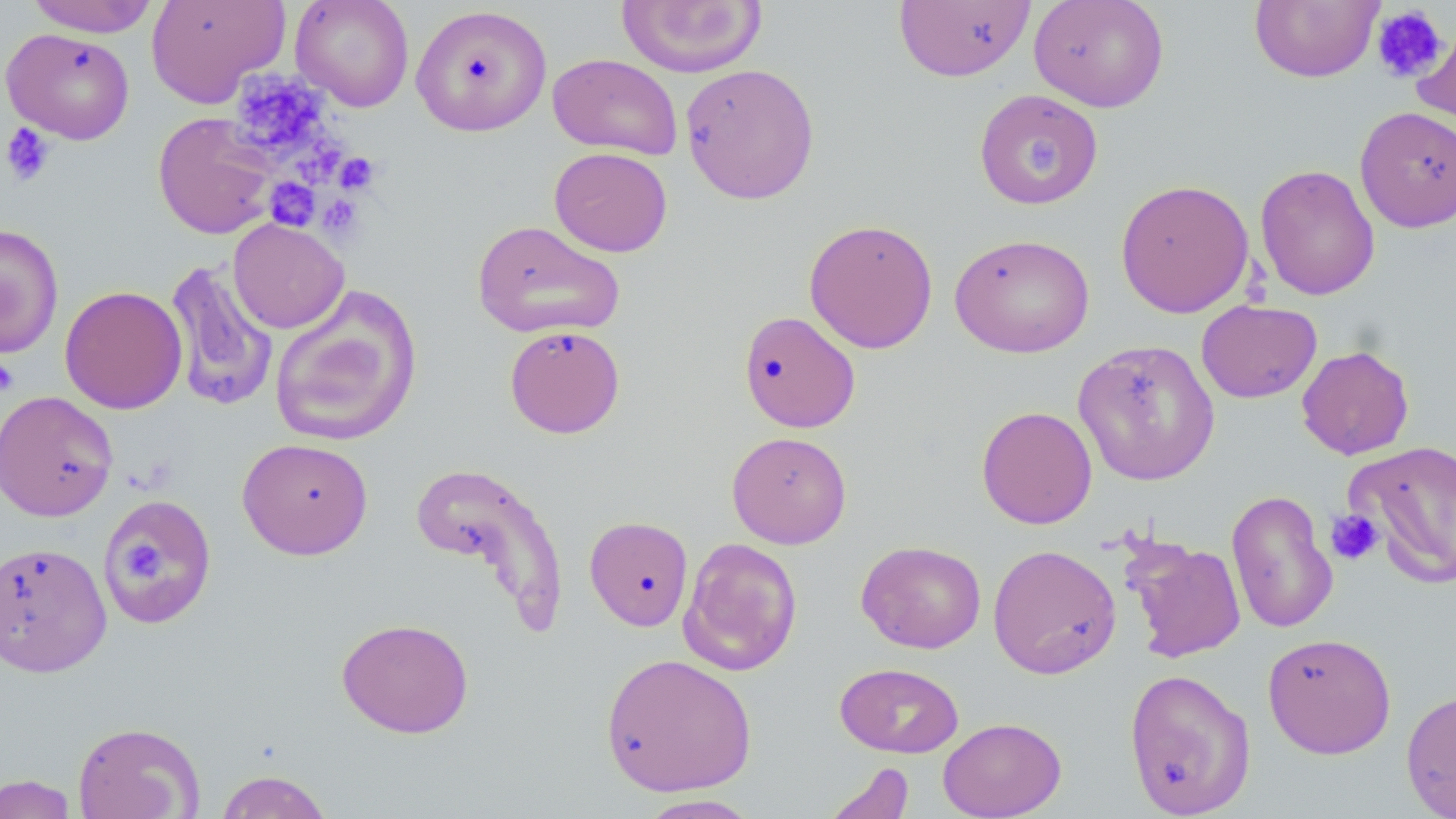 Approximate bounding boxes as (x1,y1)-(x2,y2) corner pairs in pixels. Uninfected red blood cell locations: (25,0)-(160,37), (147,0)-(289,108), (290,0)-(415,112), (1028,0)-(1169,113), (616,1)-(768,78), (893,1)-(1035,82), (1249,1)-(1384,83), (411,5)-(552,136), (1412,19)-(1456,138), (1,27)-(136,144), (548,53)-(683,160), (680,62)-(820,204), (974,89)-(1102,210), (1354,105)-(1456,233), (153,112)-(278,240), (548,147)-(673,257), (1254,163)-(1380,301), (1115,178)-(1255,319), (228,218)-(349,334), (803,218)-(938,354), (472,219)-(625,339), (0,224)-(64,359), (949,232)-(1095,358), (164,259)-(279,411), (59,285)-(188,414), (269,286)-(423,448), (1196,300)-(1322,404), (738,310)-(861,433), (504,324)-(625,438), (1072,339)-(1221,486), (1297,344)-(1414,460), (0,390)-(119,522), (976,405)-(1097,529), (727,431)-(852,548), (236,437)-(374,560), (1347,439)-(1456,587), (411,460)-(569,629), (1226,488)-(1338,635), (99,493)-(218,629), (584,515)-(693,630), (678,537)-(803,676), (1125,538)-(1247,663), (856,539)-(987,654), (0,541)-(112,677), (988,544)-(1122,680), (336,617)-(475,739), (1262,631)-(1396,760), (600,652)-(758,797), (834,662)-(964,758), (1123,667)-(1256,818), (1401,688)-(1456,818), (938,717)-(1066,819), (72,721)-(205,819), (822,761)-(914,819), (214,769)-(334,818), (0,774)-(80,818), (635,794)-(764,818). Platelet locations: (1371,5)-(1449,83), (230,70)-(328,159), (2,121)-(57,186), (1024,135)-(1068,187), (295,137)-(346,186), (334,152)-(380,194), (265,178)-(320,231), (317,194)-(364,239), (0,355)-(18,396), (1326,509)-(1385,565), (125,533)-(168,591). Slide-level diagnosis: no evidence of blood parasites. May-Grünwald-Giemsa stain. Single field of view. Captured at 1000x magnification. Image is 1456×819 pixels. Light microscopy. Thin blood smear.